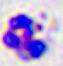

identification = white blood cell
magnification = 400x
modality = micrograph